State the preparation type.
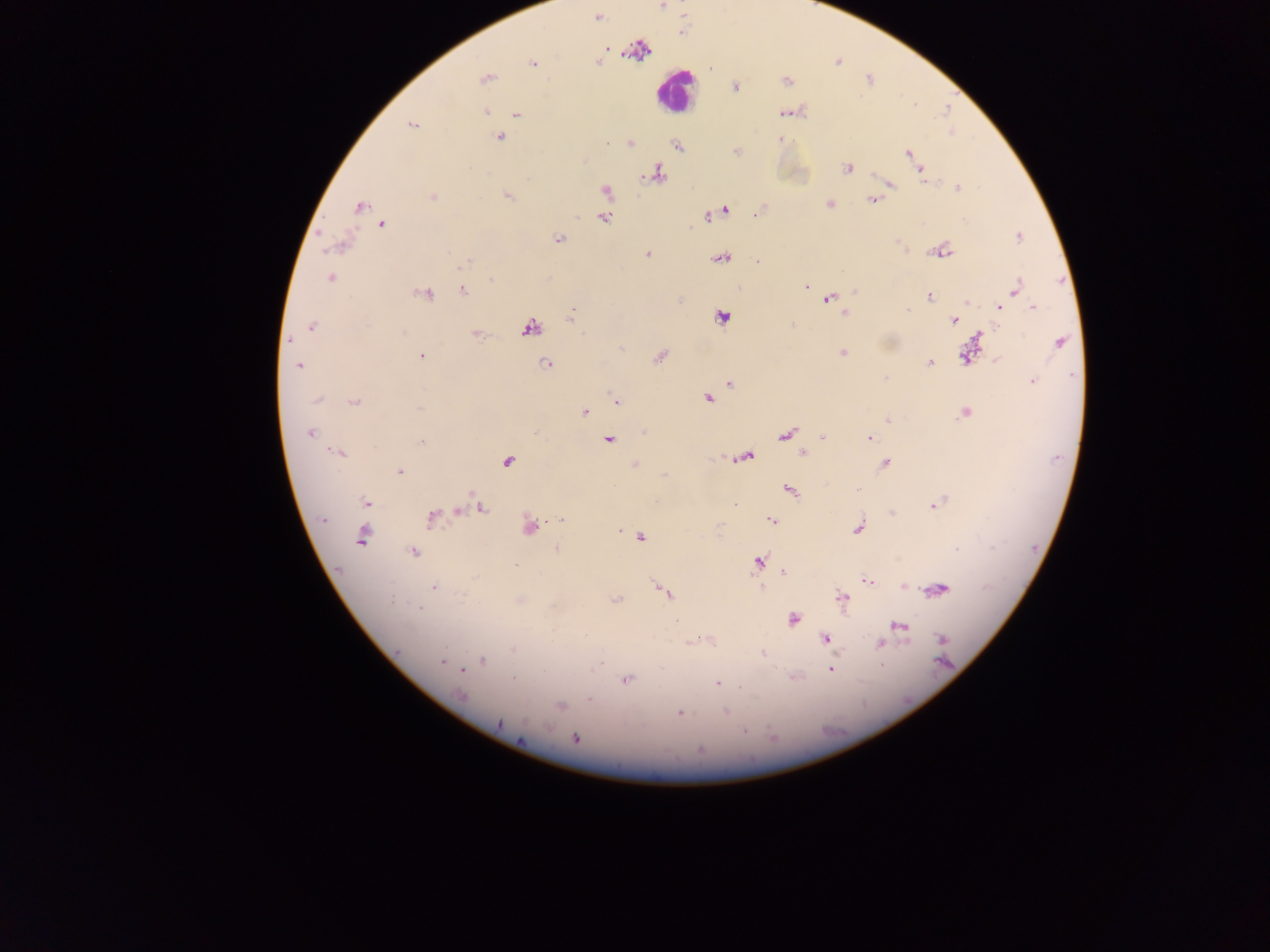
Thick blood film.

malaria parasite locations = approximate centers as {x, y} in pixels: {662, 6}, {598, 17}, {607, 49}, {637, 50}, {837, 61}, {533, 64}, {710, 68}, {486, 78}, {786, 81}, {735, 85}, {484, 110}, {788, 112}, {516, 113}, {412, 124}, {499, 137}, {781, 140}, {607, 142}, {630, 143}, {677, 145}, {736, 151}, {908, 153}, {846, 168}, {920, 171}, {656, 173}, {888, 183}, {957, 187}, {606, 190}, {506, 195}, {433, 196}, {873, 200}, {828, 203}, {359, 206}, {724, 211}, {759, 211}, {707, 215}, {602, 216}, {381, 224}, {1020, 236}, {557, 239}, {898, 242}, {339, 245}, {900, 245}, {941, 249}, {647, 254}, {721, 258}, {758, 261}, {465, 263}, {330, 277}, {491, 280}, {806, 286}, {1015, 287}, {463, 290}, {423, 293}, {929, 295}, {827, 297}, {828, 298}, {834, 304}, {998, 305}, {1034, 307}, {844, 313}, {569, 317}, {722, 317}, {954, 320}, {792, 326}, {311, 327}, {529, 327}, {476, 334}, {289, 339}, {1059, 342}, {968, 352}, {843, 353}, {421, 356}, {659, 356}, {997, 360}, {929, 362}, {546, 364}, {298, 365}, {1032, 380}, {729, 383}, {318, 398}, {709, 398}, {617, 401}, {354, 402}, {418, 408}, {583, 411}, {964, 412}, {888, 420}, {310, 432}, {645, 432}, {786, 434}, {823, 438}, {868, 438}, {608, 440}, {421, 441}, {338, 452}, {803, 452}, {743, 456}, {506, 460}, {885, 463}, {635, 465}, {399, 471}, {857, 489}, {788, 490}, {366, 502}, {733, 502}, {934, 503}, {478, 508}, {457, 511}, {892, 513}, {323, 518}, {431, 518}, {561, 520}, {771, 521}, {528, 526}, {858, 528}, {620, 529}, {361, 536}, {639, 537}, {556, 548}, {956, 550}, {412, 552}, {757, 562}, {783, 573}, {867, 580}, {903, 585}, {433, 588}, {937, 589}, {663, 591}, {615, 598}, {842, 598}, {519, 599}, {792, 618}, {677, 623}, {898, 626}, {826, 639}, {941, 639}, {697, 640}, {879, 644}, {762, 653}, {442, 661}, {482, 661}, {831, 668}, {462, 670}, {512, 678}, {625, 679}, {717, 683}, {461, 696}, {590, 699}, {559, 705}, {725, 712}, {679, 713}, {499, 723}, {575, 739}
leukocyte locations = approximate centers as {x, y} in pixels: {675, 91}
country = Ghana
capture = mobile-phone photograph through a microscope
image size = 1270×952 pixels
field of view = single